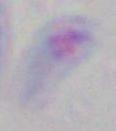
magnification: 1000x
identification: Toxoplasma gondii
modality: photomicrograph